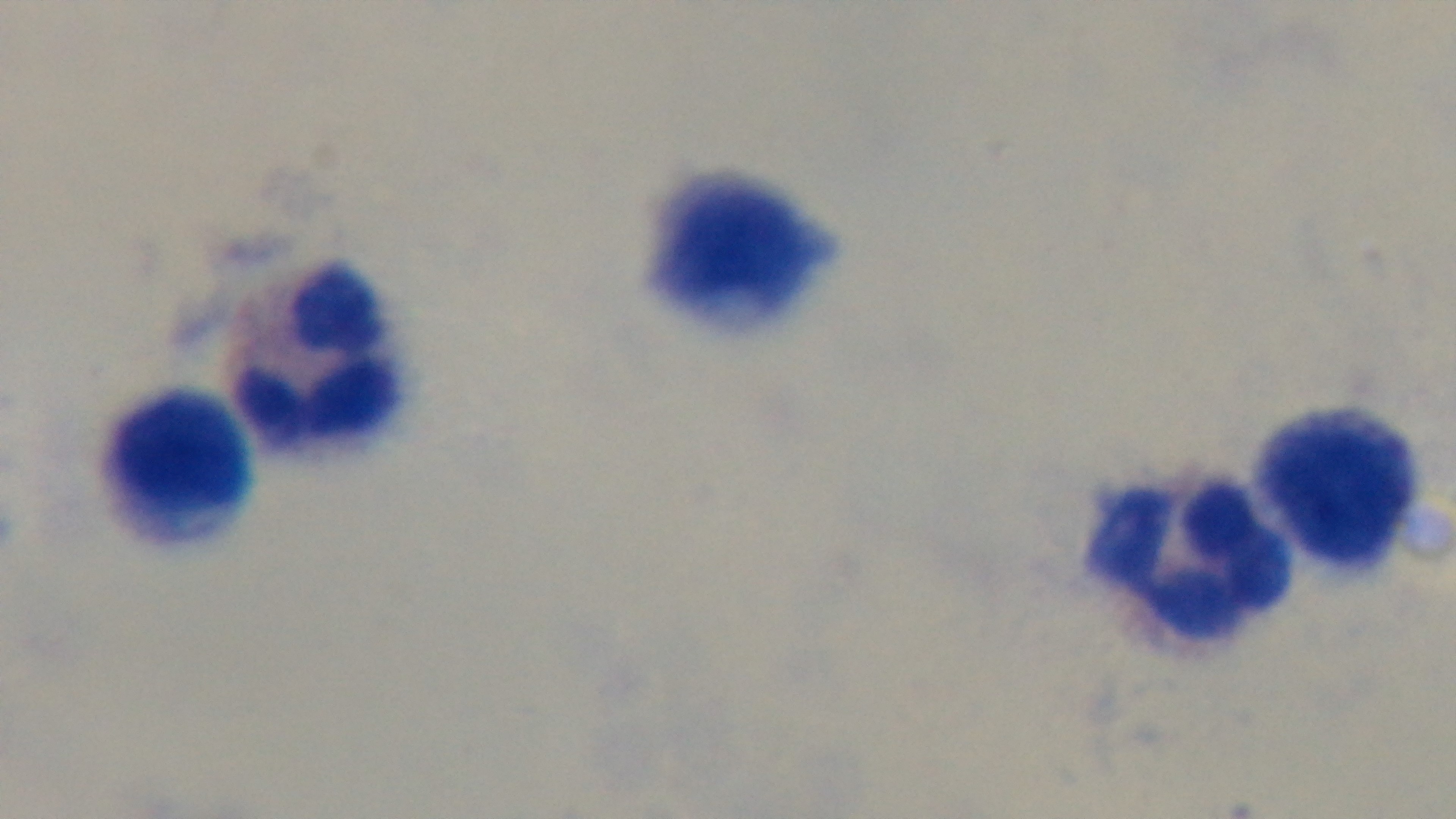 Captured with a mounted 4K digital camera. Preparation: thick smear. One field from the slide. Giemsa-stained. Oil-immersion objective, 100x. Malaria status: negative. Photomicrograph.